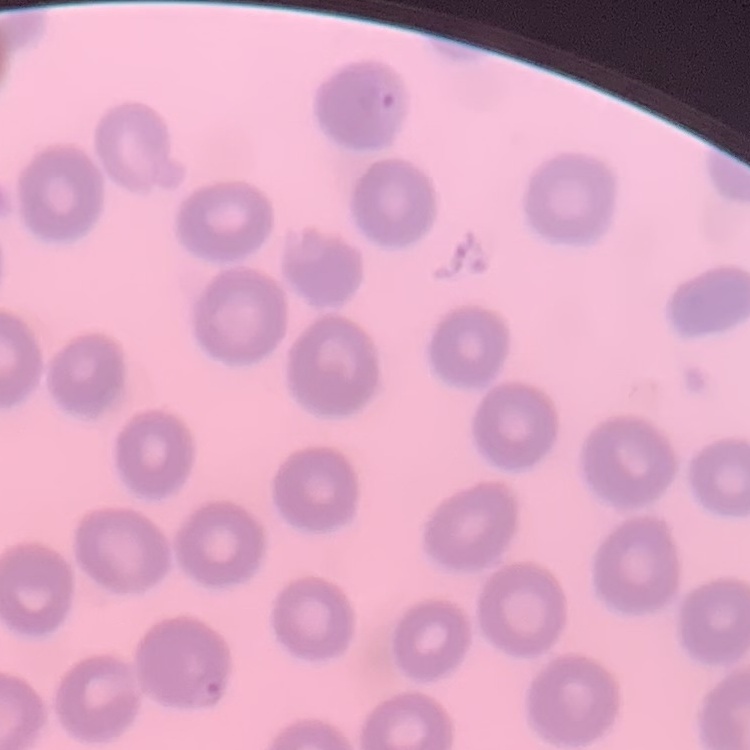
{
  "erythrocyte_morphology": "no rouleaux formation",
  "image_type": "one tile cut from a larger photomicrograph",
  "stain": "Field's or Giemsa",
  "preparation": "thin peripheral smear"
}